Identify the parasite.
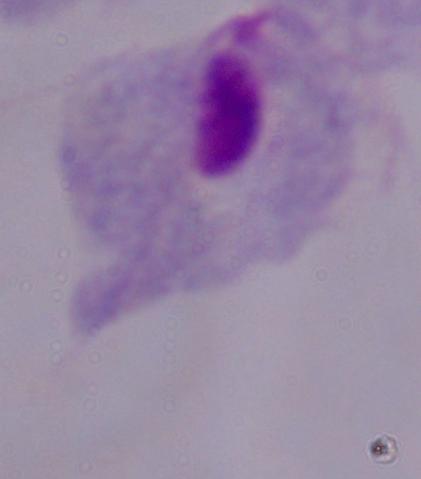
This is a trichomonad.

Micrograph. 1000x magnification.